Assess this cell for malaria.
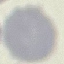
Uninfected.

image type = automatically extracted cell patch, resized to 64 × 64 pixels
preparation = thin blood smear
stain = Giemsa
capture = smartphone camera at the microscope eyepiece